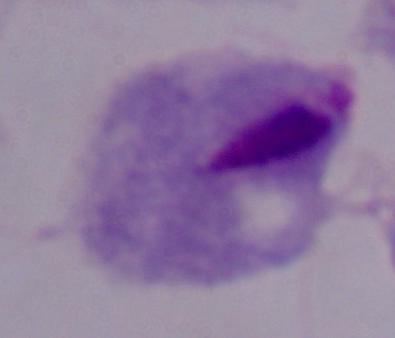

Summary:
  - Modality: micrograph
  - Magnification: 1000x
  - Identification: trichomonad